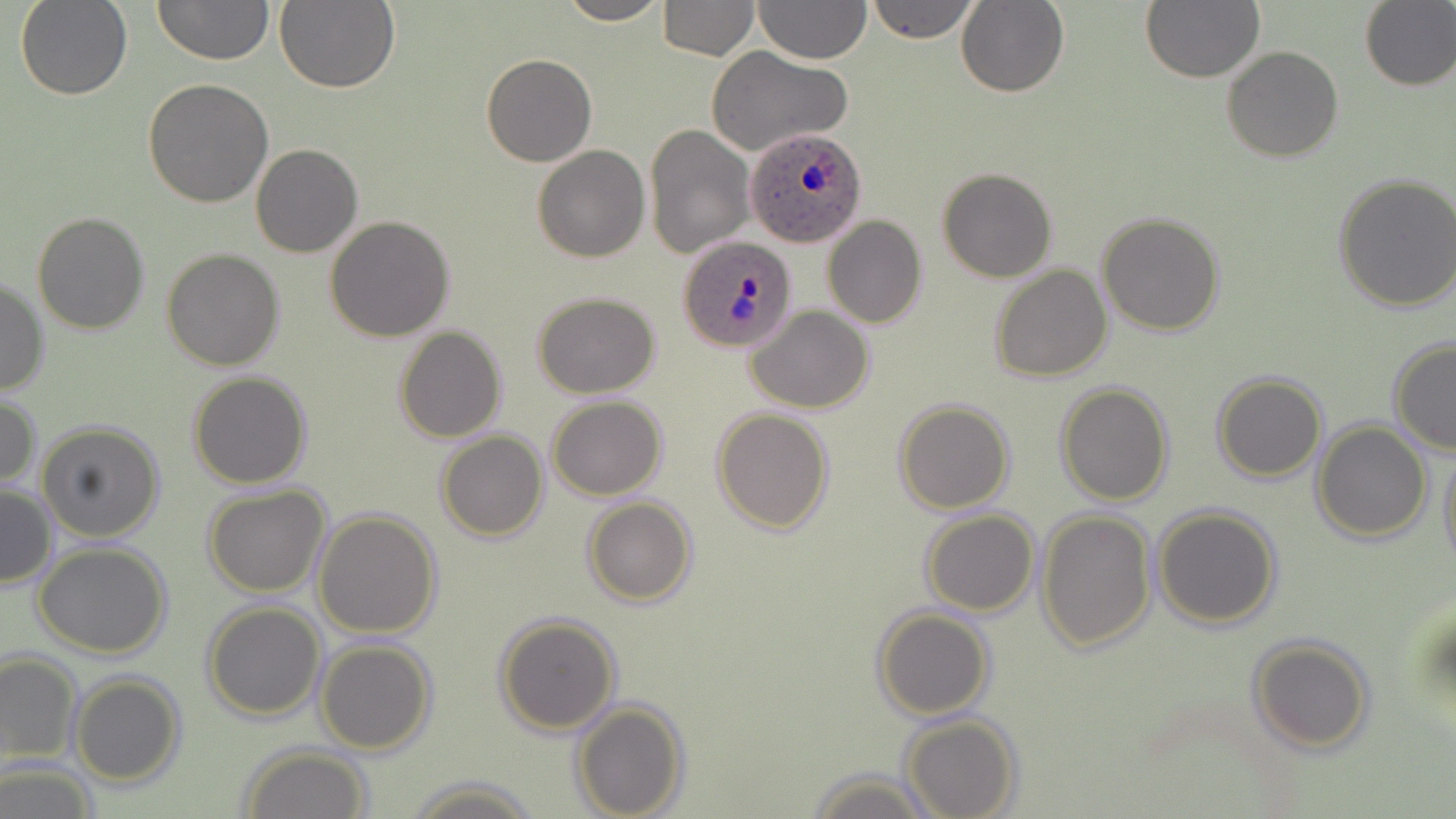

Approximate bounding boxes as named x1/y1/x2/y2 corners in pixels. Uninfected red blood cell locations: (x1=15, y1=0, x2=132, y2=100), (x1=153, y1=0, x2=273, y2=66), (x1=275, y1=0, x2=401, y2=95), (x1=555, y1=0, x2=671, y2=25), (x1=657, y1=0, x2=759, y2=59), (x1=753, y1=0, x2=871, y2=65), (x1=866, y1=0, x2=980, y2=44), (x1=1142, y1=0, x2=1265, y2=83), (x1=957, y1=1, x2=1070, y2=97), (x1=1358, y1=1, x2=1456, y2=91), (x1=1222, y1=46, x2=1344, y2=162), (x1=707, y1=47, x2=851, y2=157), (x1=481, y1=53, x2=596, y2=167), (x1=143, y1=79, x2=274, y2=206), (x1=644, y1=122, x2=756, y2=259), (x1=250, y1=144, x2=363, y2=258), (x1=532, y1=145, x2=650, y2=262), (x1=936, y1=166, x2=1057, y2=282), (x1=1333, y1=172, x2=1456, y2=312), (x1=31, y1=210, x2=152, y2=334), (x1=1096, y1=212, x2=1225, y2=336), (x1=325, y1=215, x2=455, y2=341), (x1=824, y1=216, x2=927, y2=329), (x1=161, y1=247, x2=285, y2=370), (x1=170, y1=250, x2=295, y2=489), (x1=990, y1=265, x2=1112, y2=382), (x1=0, y1=276, x2=49, y2=397), (x1=532, y1=292, x2=660, y2=398), (x1=747, y1=306, x2=876, y2=414), (x1=392, y1=325, x2=508, y2=442), (x1=1388, y1=338, x2=1456, y2=455), (x1=188, y1=371, x2=312, y2=489), (x1=1212, y1=371, x2=1327, y2=482), (x1=1054, y1=382, x2=1175, y2=505), (x1=0, y1=393, x2=40, y2=491), (x1=547, y1=396, x2=667, y2=500), (x1=894, y1=398, x2=1015, y2=514), (x1=712, y1=408, x2=834, y2=532), (x1=1311, y1=420, x2=1433, y2=543), (x1=36, y1=421, x2=165, y2=542), (x1=435, y1=430, x2=549, y2=541), (x1=1438, y1=439, x2=1456, y2=573), (x1=0, y1=483, x2=57, y2=589), (x1=203, y1=485, x2=331, y2=597), (x1=582, y1=497, x2=698, y2=606), (x1=1152, y1=504, x2=1282, y2=629), (x1=313, y1=508, x2=443, y2=638), (x1=920, y1=509, x2=1039, y2=616), (x1=1037, y1=509, x2=1156, y2=653), (x1=33, y1=543, x2=172, y2=659), (x1=202, y1=600, x2=326, y2=720), (x1=873, y1=606, x2=992, y2=720), (x1=493, y1=613, x2=622, y2=735), (x1=1247, y1=636, x2=1375, y2=754), (x1=314, y1=639, x2=436, y2=754), (x1=0, y1=650, x2=82, y2=766), (x1=69, y1=674, x2=186, y2=786), (x1=571, y1=698, x2=688, y2=818), (x1=899, y1=714, x2=1021, y2=819), (x1=238, y1=745, x2=373, y2=819), (x1=0, y1=761, x2=99, y2=818), (x1=808, y1=768, x2=936, y2=819), (x1=402, y1=778, x2=544, y2=819). Plasmodium ovale-infected red blood cell locations: (x1=745, y1=125, x2=868, y2=248), (x1=678, y1=234, x2=797, y2=353). Slide-level diagnosis: Plasmodium ovale. Thin blood film. May-Grünwald-Giemsa stain. Optical microscopy. One field of a larger specimen. Image is 1456×819 pixels. 1000x magnification.